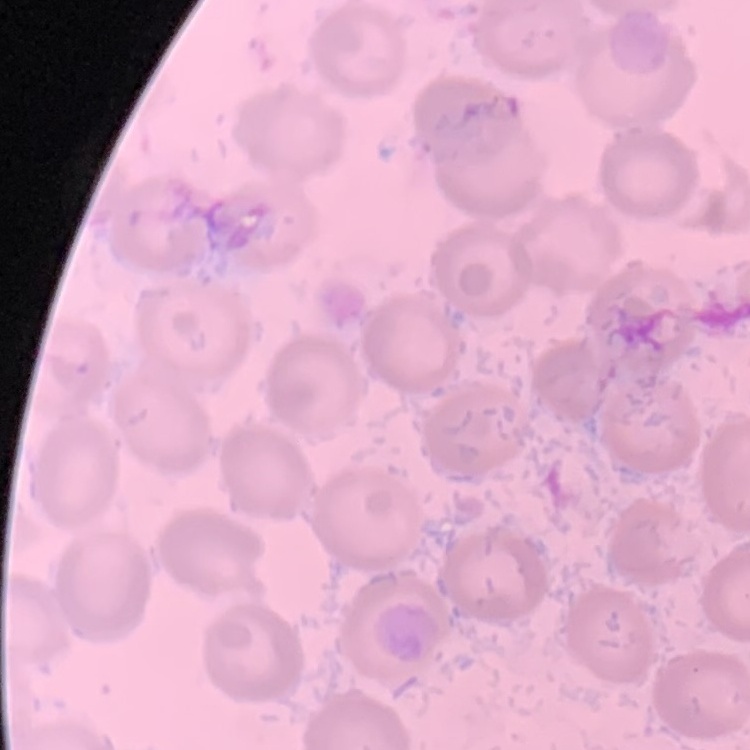

erythrocyte_morphology: no rouleaux formation
stain: Field's or Giemsa
image_type: square crop of a larger photomicrograph
preparation: thin peripheral smear